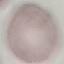

Summary:
  - Result: no malaria parasites detected
  - Image type: automatically extracted cell patch, resized to 64 × 64 pixels
  - Preparation: thin blood smear
  - Capture: smartphone through the microscope eyepiece
  - Stain: Giemsa